Locate every uninfected red blood cell.
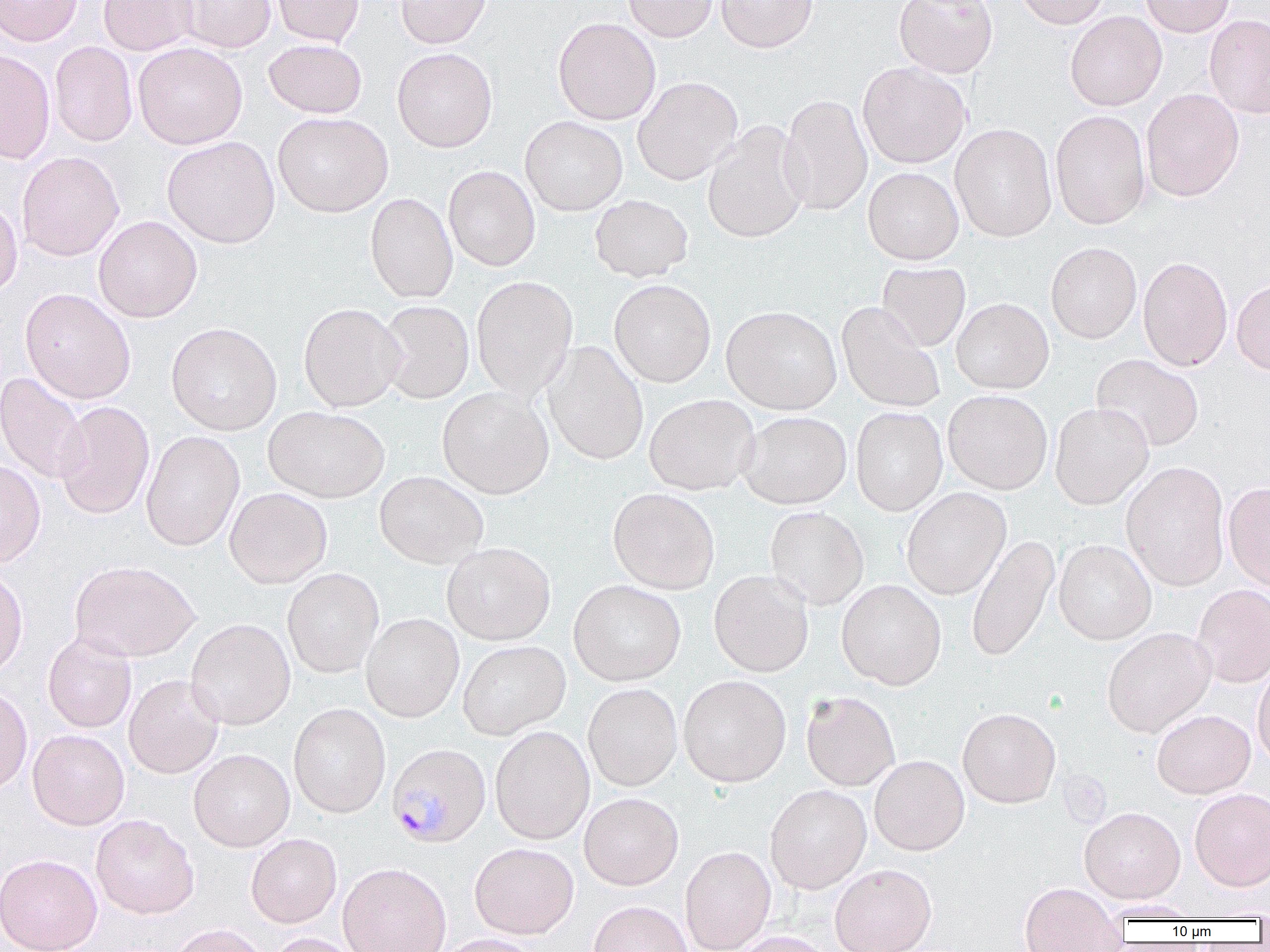
Approximate bounding boxes as [x1, y1, x2, y2] in pixels.
Uninfected red blood cells: [0, 0, 83, 46], [99, 0, 197, 55], [176, 0, 276, 52], [271, 0, 365, 46], [395, 0, 491, 48], [623, 0, 718, 42], [716, 0, 817, 52], [894, 0, 998, 78], [1014, 0, 1110, 29], [1140, 0, 1235, 37], [1065, 11, 1166, 111], [1204, 14, 1270, 118], [553, 17, 660, 125], [263, 39, 367, 118], [50, 41, 138, 147], [133, 42, 247, 148], [392, 47, 497, 152], [0, 50, 56, 164], [858, 61, 971, 168], [633, 76, 742, 185], [1141, 88, 1244, 201], [779, 94, 872, 216], [1050, 110, 1151, 229], [272, 112, 393, 217], [520, 116, 628, 215], [950, 123, 1057, 242], [702, 124, 809, 244], [162, 136, 280, 248], [17, 151, 124, 261], [443, 166, 540, 271], [863, 167, 964, 265], [365, 192, 458, 303], [589, 194, 694, 282], [0, 197, 23, 299], [93, 216, 202, 322], [1046, 242, 1142, 344], [1138, 256, 1233, 371], [877, 262, 970, 352], [471, 275, 578, 401], [609, 279, 716, 387], [1232, 279, 1270, 375], [20, 288, 136, 404], [951, 298, 1054, 394], [376, 300, 474, 404], [836, 302, 945, 413], [298, 303, 405, 411], [721, 305, 842, 414], [166, 322, 282, 435], [543, 341, 649, 466], [1091, 354, 1204, 452], [0, 372, 90, 485], [437, 387, 554, 499], [943, 390, 1052, 494], [644, 394, 759, 495], [54, 401, 154, 520], [1050, 402, 1154, 509], [263, 406, 390, 503], [851, 407, 948, 515], [738, 412, 852, 509], [141, 431, 244, 551], [0, 459, 45, 569], [1121, 462, 1229, 591], [374, 471, 488, 569], [1223, 481, 1270, 591], [901, 487, 1011, 600], [224, 488, 332, 588], [607, 488, 720, 594], [765, 506, 869, 610], [965, 533, 1060, 663], [1054, 540, 1157, 645], [441, 542, 556, 646], [69, 561, 200, 663], [0, 568, 28, 680], [282, 568, 384, 678], [709, 570, 814, 677], [836, 579, 946, 689], [568, 580, 686, 685], [1192, 584, 1270, 687], [361, 614, 464, 722], [185, 619, 295, 730], [1102, 627, 1215, 737], [42, 632, 137, 734], [458, 641, 571, 739], [1252, 661, 1270, 769], [123, 675, 224, 779], [678, 675, 792, 787], [582, 683, 682, 791], [0, 684, 32, 795], [800, 690, 901, 791], [288, 704, 391, 818], [957, 707, 1061, 808], [1151, 709, 1255, 798], [490, 726, 595, 845], [28, 729, 129, 830], [188, 749, 295, 851], [869, 755, 969, 855], [765, 784, 871, 893], [1189, 788, 1270, 891], [579, 793, 683, 890], [1079, 806, 1185, 902], [91, 814, 199, 919], [245, 833, 342, 929], [469, 843, 579, 939], [680, 846, 776, 951], [0, 853, 102, 952], [337, 862, 451, 952], [830, 864, 937, 952], [1019, 882, 1125, 952], [588, 901, 692, 952], [168, 923, 270, 952], [729, 931, 833, 952], [267, 932, 363, 952], [432, 934, 541, 952].

Plasmodium malariae-infected red blood cell locations: [386, 741, 491, 846]. Slide-level diagnosis: Plasmodium malariae. Light microscopy. Single field of view. Thin blood smear. Image is 1270×952 pixels. Captured at 1000x magnification.